Name the blood parasite species.
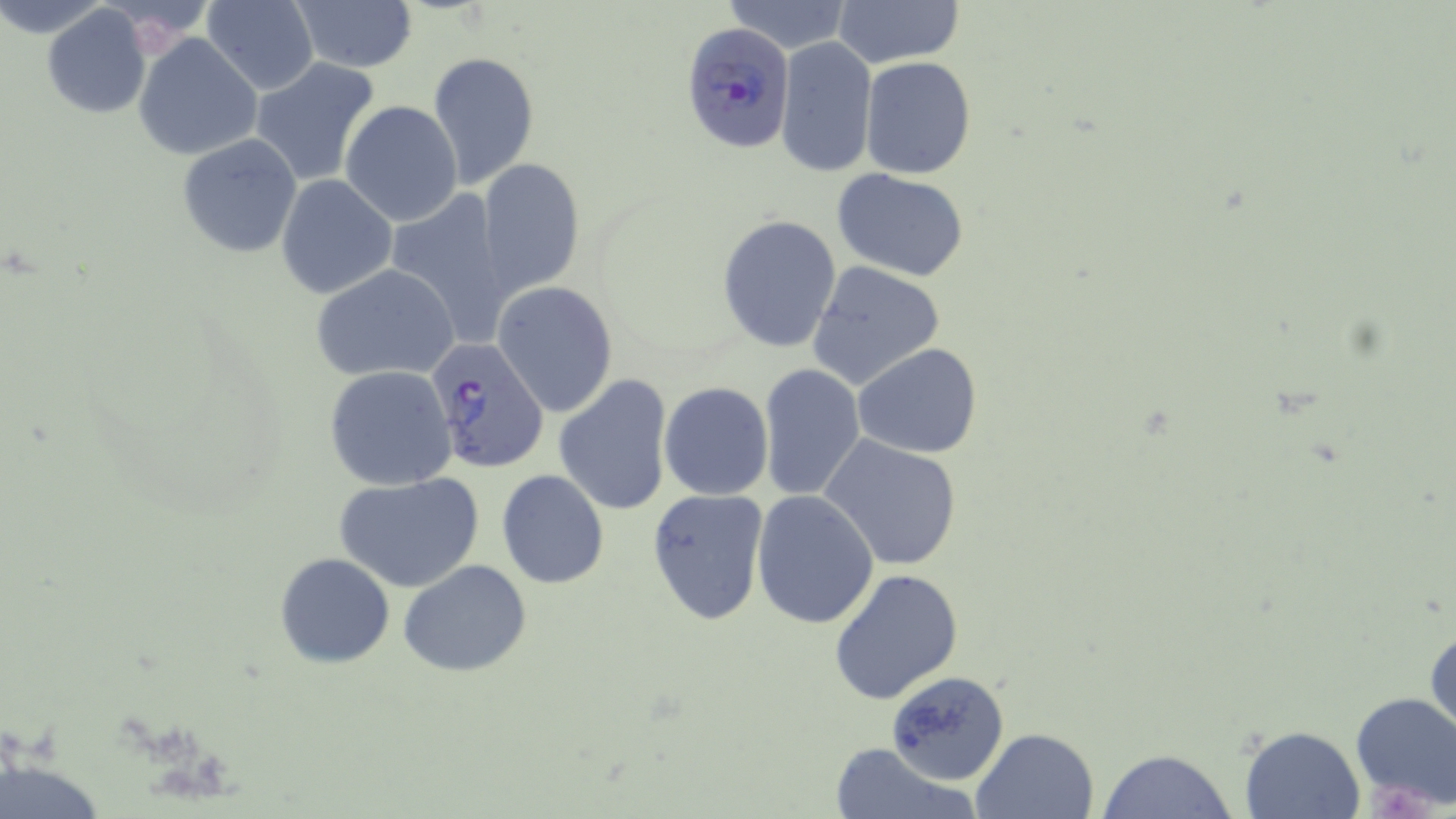

Plasmodium falciparum.

Approximate bounding boxes as named x1/y1/x2/y2 corners in pixels. Platelet locations: (x1=1348, y1=691, x2=1456, y2=813). Plasmodium falciparum-infected red blood cell locations: (x1=684, y1=23, x2=799, y2=151), (x1=426, y1=337, x2=550, y2=472). White blood cell locations: (x1=1367, y1=782, x2=1434, y2=819). Uninfected red blood cell locations: (x1=203, y1=0, x2=320, y2=94), (x1=722, y1=0, x2=854, y2=52), (x1=834, y1=0, x2=963, y2=69), (x1=290, y1=1, x2=418, y2=74), (x1=41, y1=4, x2=151, y2=118), (x1=133, y1=33, x2=259, y2=160), (x1=776, y1=36, x2=877, y2=178), (x1=427, y1=51, x2=539, y2=190), (x1=860, y1=56, x2=975, y2=179), (x1=250, y1=57, x2=381, y2=187), (x1=341, y1=100, x2=462, y2=227), (x1=177, y1=133, x2=301, y2=258), (x1=477, y1=158, x2=585, y2=295), (x1=831, y1=168, x2=970, y2=279), (x1=277, y1=175, x2=395, y2=298), (x1=383, y1=189, x2=514, y2=347), (x1=717, y1=215, x2=841, y2=352), (x1=807, y1=261, x2=947, y2=394), (x1=314, y1=265, x2=460, y2=381), (x1=493, y1=282, x2=618, y2=416), (x1=853, y1=343, x2=983, y2=459), (x1=758, y1=362, x2=866, y2=502), (x1=324, y1=365, x2=458, y2=490), (x1=555, y1=374, x2=672, y2=517), (x1=658, y1=382, x2=774, y2=501), (x1=820, y1=435, x2=964, y2=572), (x1=497, y1=469, x2=608, y2=589), (x1=333, y1=473, x2=483, y2=593), (x1=648, y1=487, x2=770, y2=625), (x1=750, y1=491, x2=879, y2=630), (x1=276, y1=553, x2=394, y2=668), (x1=399, y1=559, x2=532, y2=678), (x1=830, y1=566, x2=964, y2=706), (x1=1425, y1=617, x2=1455, y2=747), (x1=881, y1=667, x2=1010, y2=789), (x1=1240, y1=725, x2=1365, y2=817), (x1=972, y1=727, x2=1098, y2=818), (x1=828, y1=742, x2=974, y2=819), (x1=1097, y1=749, x2=1239, y2=819), (x1=0, y1=752, x2=108, y2=819). May-Grünwald-Giemsa stain. Optical microscopy. Thin blood smear. Image is 1456×819 pixels. Captured at 1000x magnification. Single field of view.